Classify this cell by malaria status.
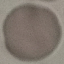

It is uninfected.

Summary:
  - Stain: Giemsa
  - Image type: automatically extracted cell patch, resized to 64 × 64 pixels
  - Preparation: thin blood smear
  - Capture: smartphone through the microscope eyepiece